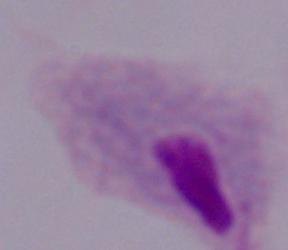
Summary:
  - Identification: trichomonad
  - Magnification: 1000x
  - Modality: micrograph